Describe the morphology of the red blood cells.
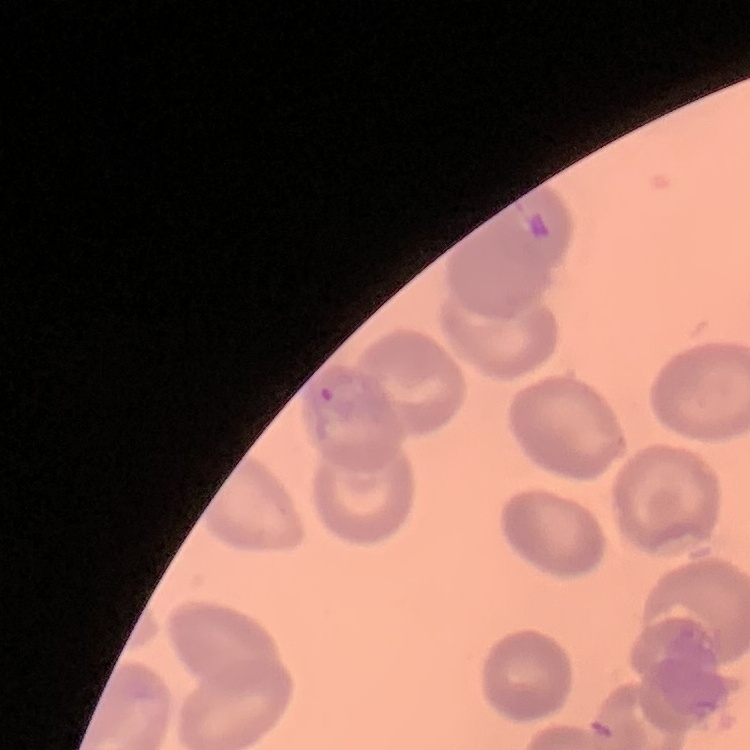
They show no rouleaux formation.

Summary:
  - Image type: square crop of a larger photomicrograph
  - Stain: Field's or Giemsa
  - Preparation: thin blood smear